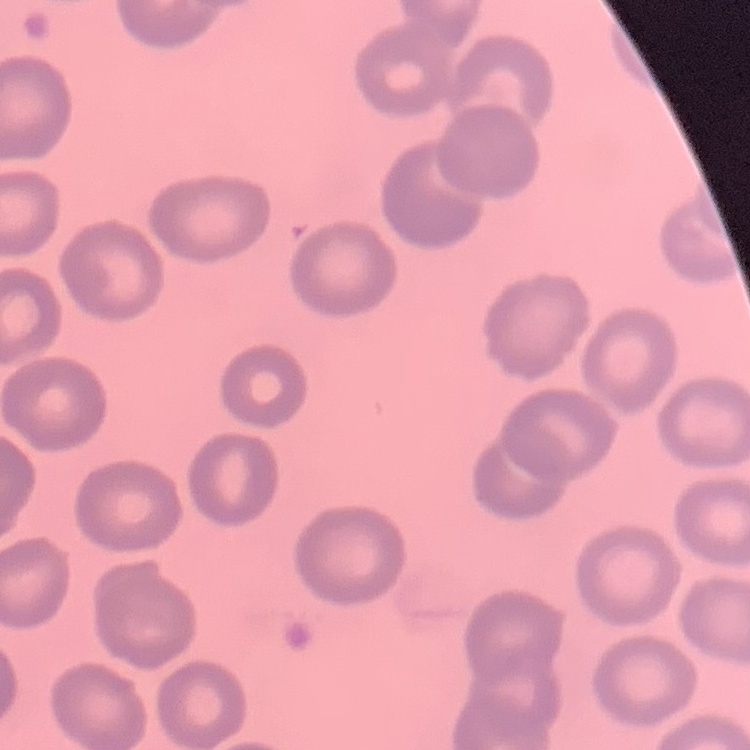
{
  "erythrocyte_morphology": "no rouleaux formation",
  "preparation": "thin blood film",
  "stain": "Field's or Giemsa",
  "image_type": "one tile cut from a larger photomicrograph"
}